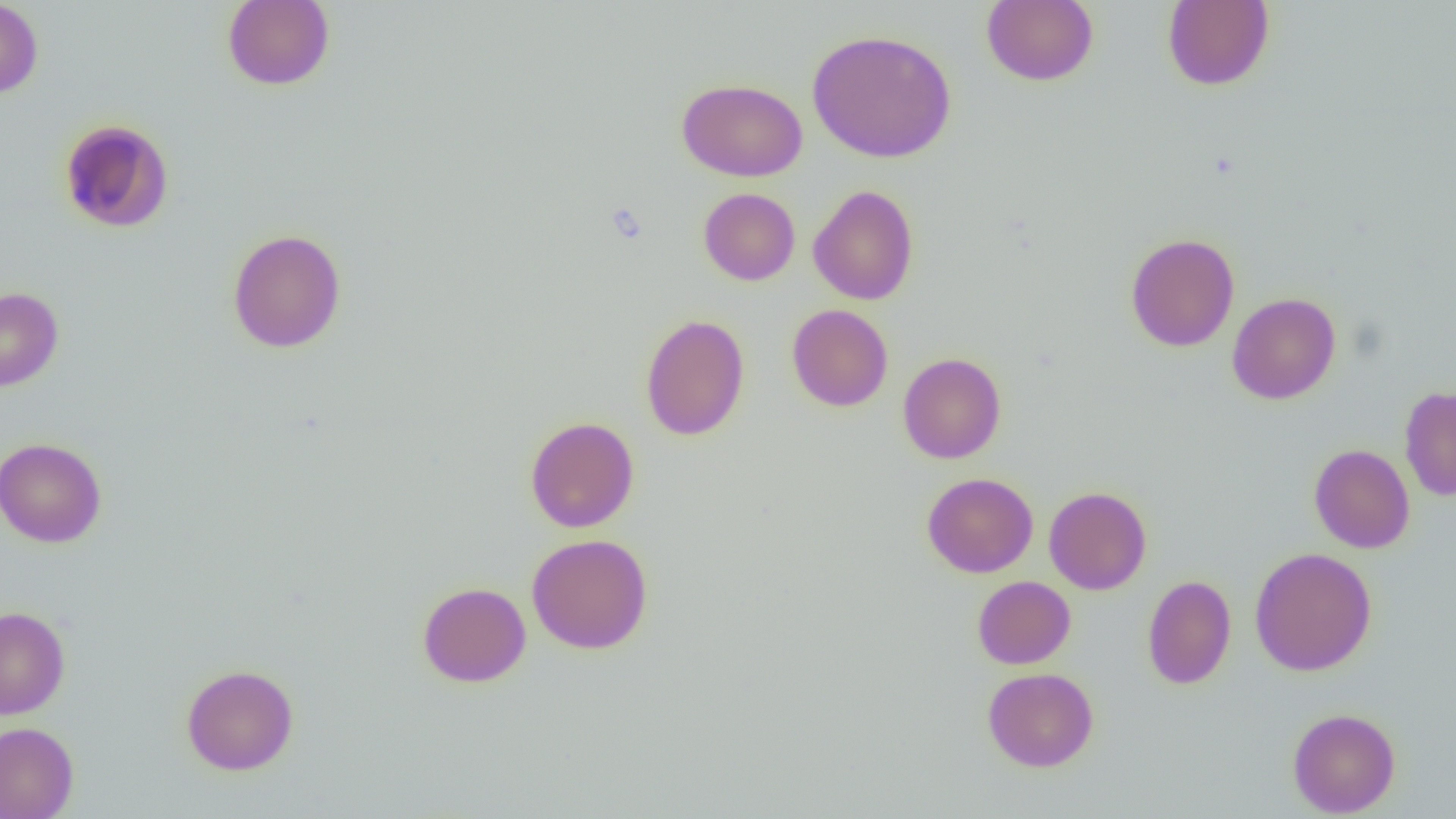

slide-level diagnosis = negative for blood parasites
modality = optical microscopy
image size = 1456×819 pixels
field of view = single
uninfected red blood cell locations = approximate bounding boxes as [x1, y1, x2, y2] in pixels: [0, 0, 43, 100], [222, 0, 335, 91], [982, 0, 1098, 86], [1162, 0, 1275, 91], [806, 28, 957, 163], [677, 78, 808, 181], [58, 118, 174, 233], [808, 184, 919, 305], [698, 188, 800, 285], [228, 228, 346, 353], [1125, 232, 1240, 352], [0, 288, 63, 391], [1227, 292, 1341, 405], [787, 304, 893, 411], [640, 314, 750, 441], [897, 352, 1006, 464], [1399, 386, 1456, 501], [524, 416, 639, 532], [0, 437, 107, 548], [1309, 444, 1415, 553], [922, 472, 1038, 577], [1043, 486, 1152, 595], [526, 533, 653, 654], [1249, 547, 1377, 676], [1142, 574, 1236, 690], [972, 576, 1075, 669], [417, 581, 531, 687], [0, 606, 70, 719], [181, 664, 299, 775], [983, 667, 1099, 772], [1287, 708, 1401, 817], [0, 721, 79, 818]
preparation = thin blood smear
magnification = 1000x